Comment on the morphology of the red blood cells.
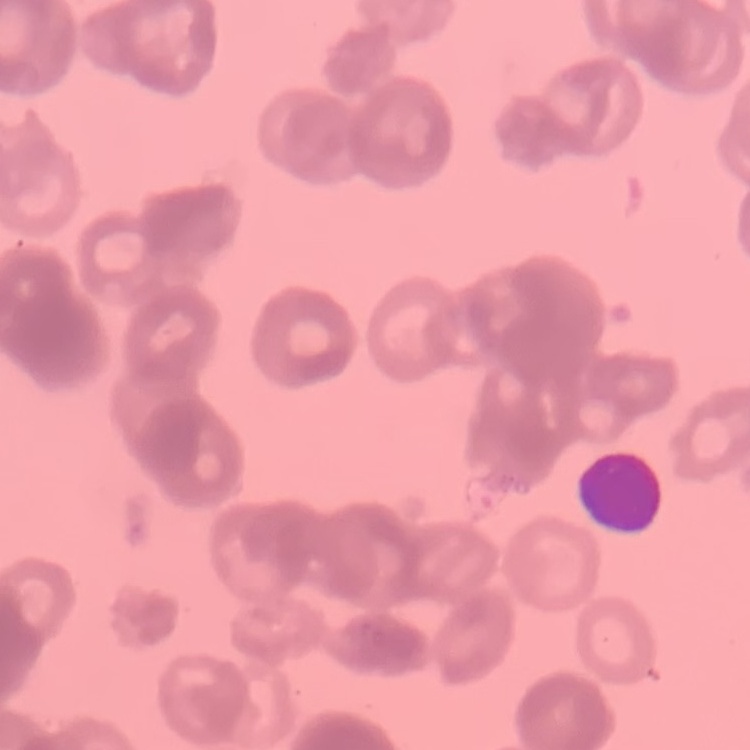

They show rouleaux formation.

Stained with either Field's or Giemsa. Square crop of a larger photomicrograph. Thin blood smear.